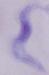
A trypanosome is seen. 1000x magnification. Photomicrograph.